State which parasite is depicted.
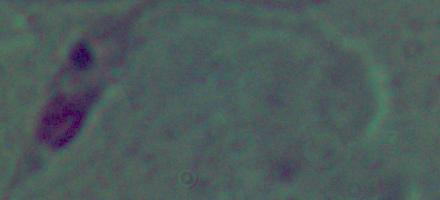
This is Leishmania.

Photomicrograph. Captured at 1000x magnification.